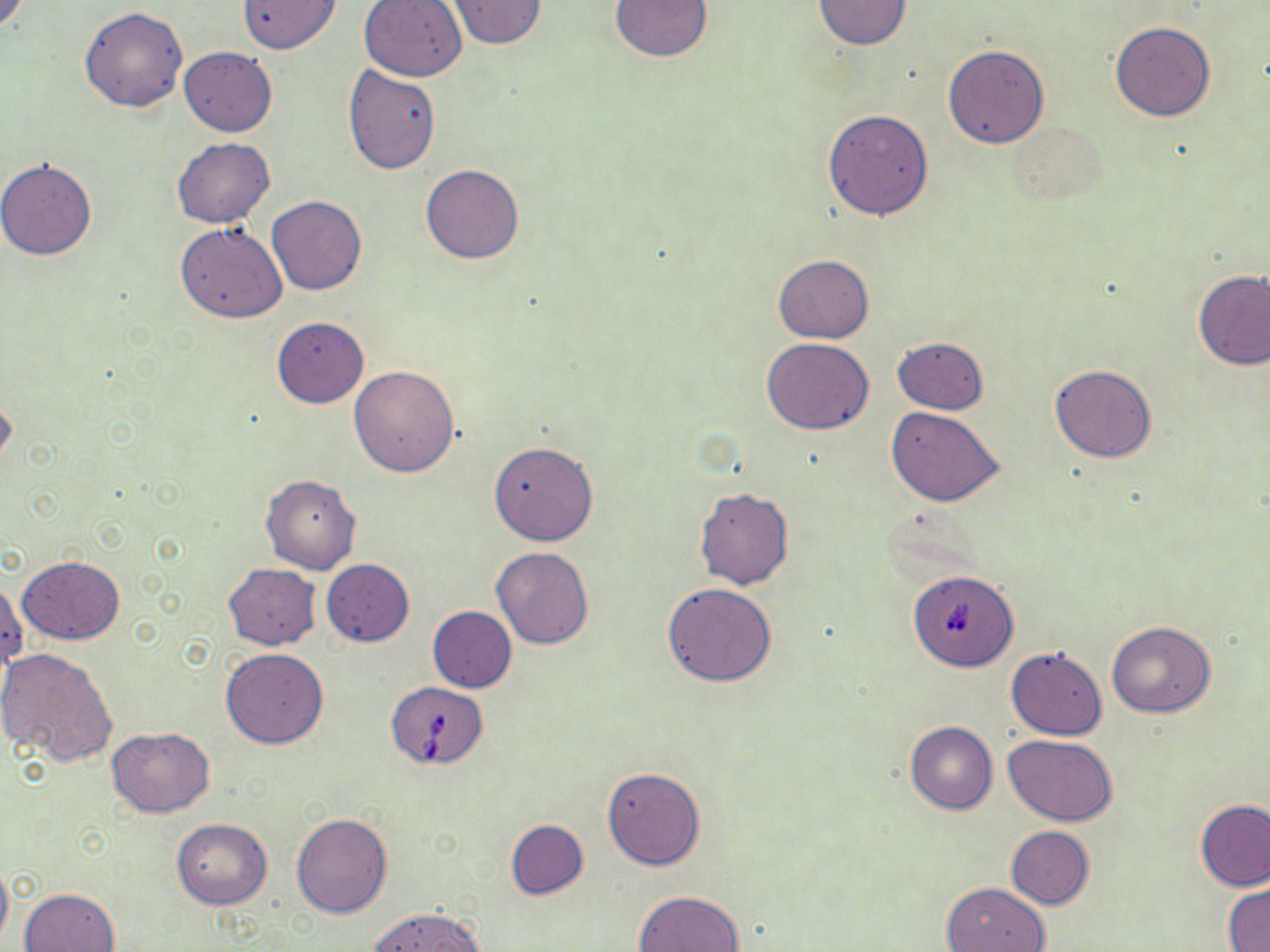
Approximate bounding boxes as (x1,y1)-(x2,y2) corner pairs in pixels. Babesia divergens-infected red blood cell locations: (903,571)-(1020,672), (386,682)-(489,769). Uninfected red blood cell locations: (446,0)-(546,50), (611,0)-(711,61), (812,0)-(912,49), (237,1)-(341,53), (358,1)-(468,82), (80,6)-(188,112), (1110,21)-(1216,121), (942,45)-(1050,148), (179,47)-(277,136), (344,64)-(441,174), (822,108)-(934,220), (1008,121)-(1109,209), (172,138)-(275,228), (0,158)-(97,260), (422,165)-(523,264), (266,196)-(367,295), (176,224)-(287,324), (772,254)-(874,343), (1194,271)-(1270,371), (271,316)-(369,407), (891,337)-(989,414), (763,338)-(874,434), (349,364)-(461,477), (1049,365)-(1157,464), (0,392)-(16,472), (886,406)-(1004,506), (489,441)-(598,545), (260,473)-(361,574), (694,488)-(793,589), (492,547)-(594,650), (18,555)-(124,643), (322,559)-(414,646), (223,563)-(320,650), (662,583)-(776,687), (428,605)-(517,692), (1107,620)-(1215,718), (0,647)-(119,766), (1005,647)-(1107,739), (220,648)-(329,749), (905,720)-(998,814), (106,727)-(216,817), (1003,734)-(1117,827), (602,767)-(706,870), (1196,800)-(1270,891), (292,812)-(392,918), (172,819)-(272,909), (506,819)-(587,900), (1006,826)-(1095,909), (0,859)-(12,949), (940,882)-(1049,951), (1223,884)-(1269,952), (21,888)-(119,952), (634,890)-(745,952), (365,907)-(486,952). Slide-level diagnosis: Babesia divergens. 1000x magnification. May-Grünwald-Giemsa-stained preparation. One field of a larger specimen. Optical microscopy. Thin blood film. Image is 1270×952 pixels.